Classify this cell by malaria status.
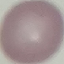

Uninfected.

Cell patch, automatically extracted from a larger field of view and resized to 64 × 64 pixels. Giemsa stain. Photographed with a smartphone camera at the microscope eyepiece. Thin smear of blood.